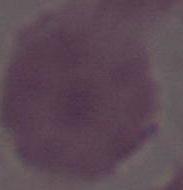

Summary:
  - Modality: micrograph
  - Magnification: 1000x
  - Identification: red blood cell